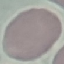
result: no malaria parasites detected
image_type: automatically extracted cell patch, resized to 64 × 64 pixels
capture: smartphone through the microscope eyepiece
stain: Giemsa
preparation: thin blood film